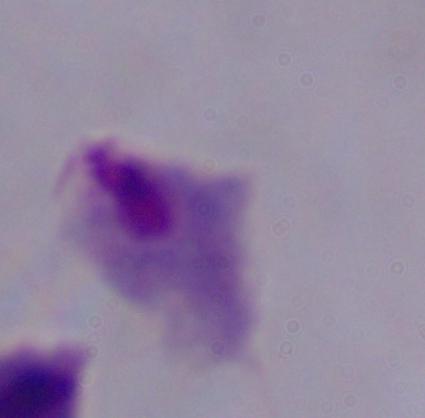

{
  "identification": "trichomonad",
  "magnification": "1000x",
  "modality": "micrograph"
}